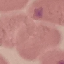
Malaria status: uninfected. Photographed with a smartphone camera at the microscope eyepiece. Thin blood smear. Giemsa-stained preparation. Automatically extracted cell patch, resized to 64 × 64 pixels.